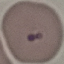
Summary:
  - Malaria status: uninfected
  - Capture: smartphone camera at the microscope eyepiece
  - Stain: Giemsa
  - Image type: cell patch, automatically extracted from a larger field of view and resized to 64 × 64 pixels
  - Preparation: thin blood smear